Give the preparation type.
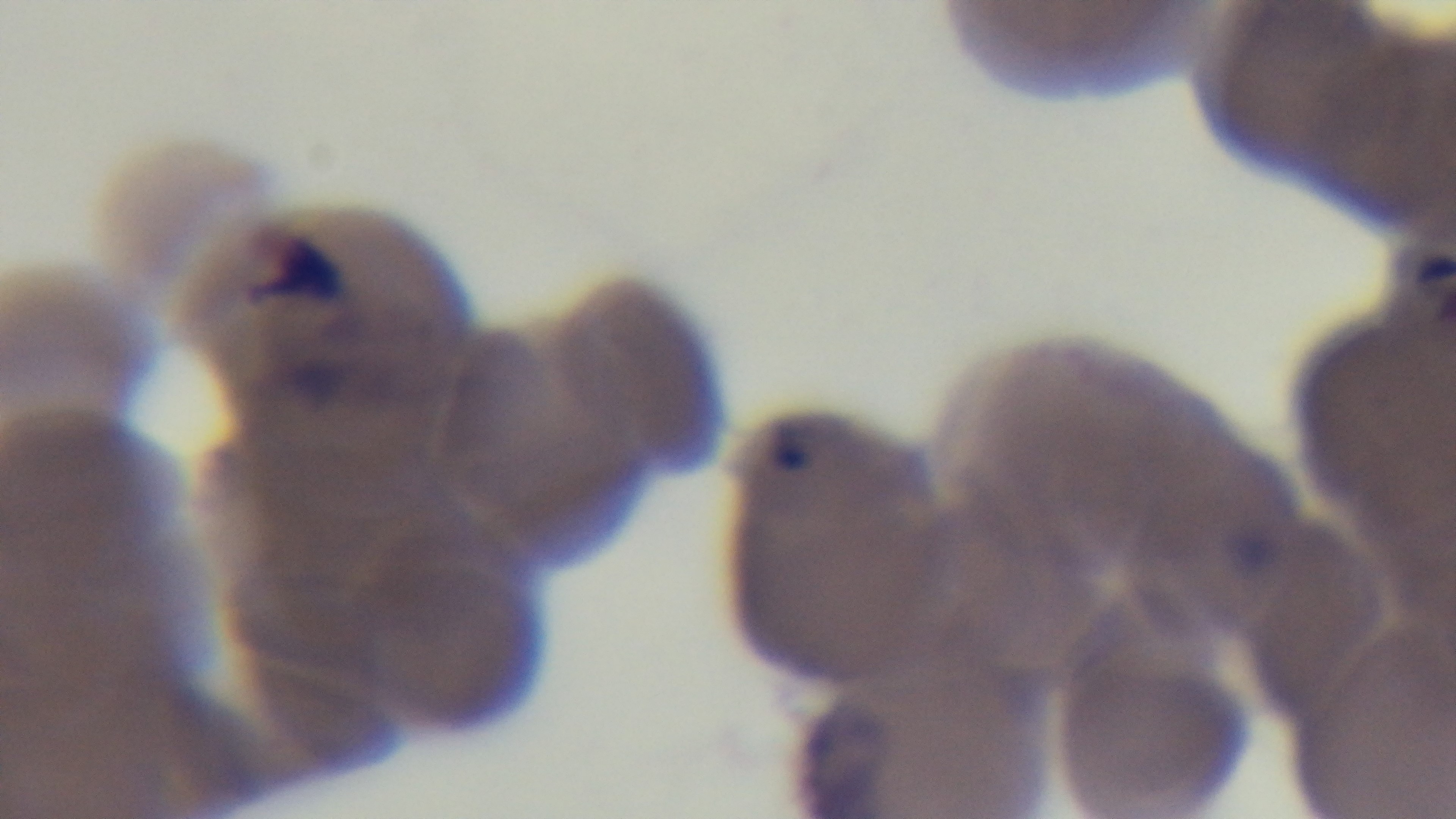
A thin smear.

100x oil-immersion objective. Light microscopy. Giemsa-stained. Captured with a mounted 4K digital camera. Malaria status: infected. Single field of view.